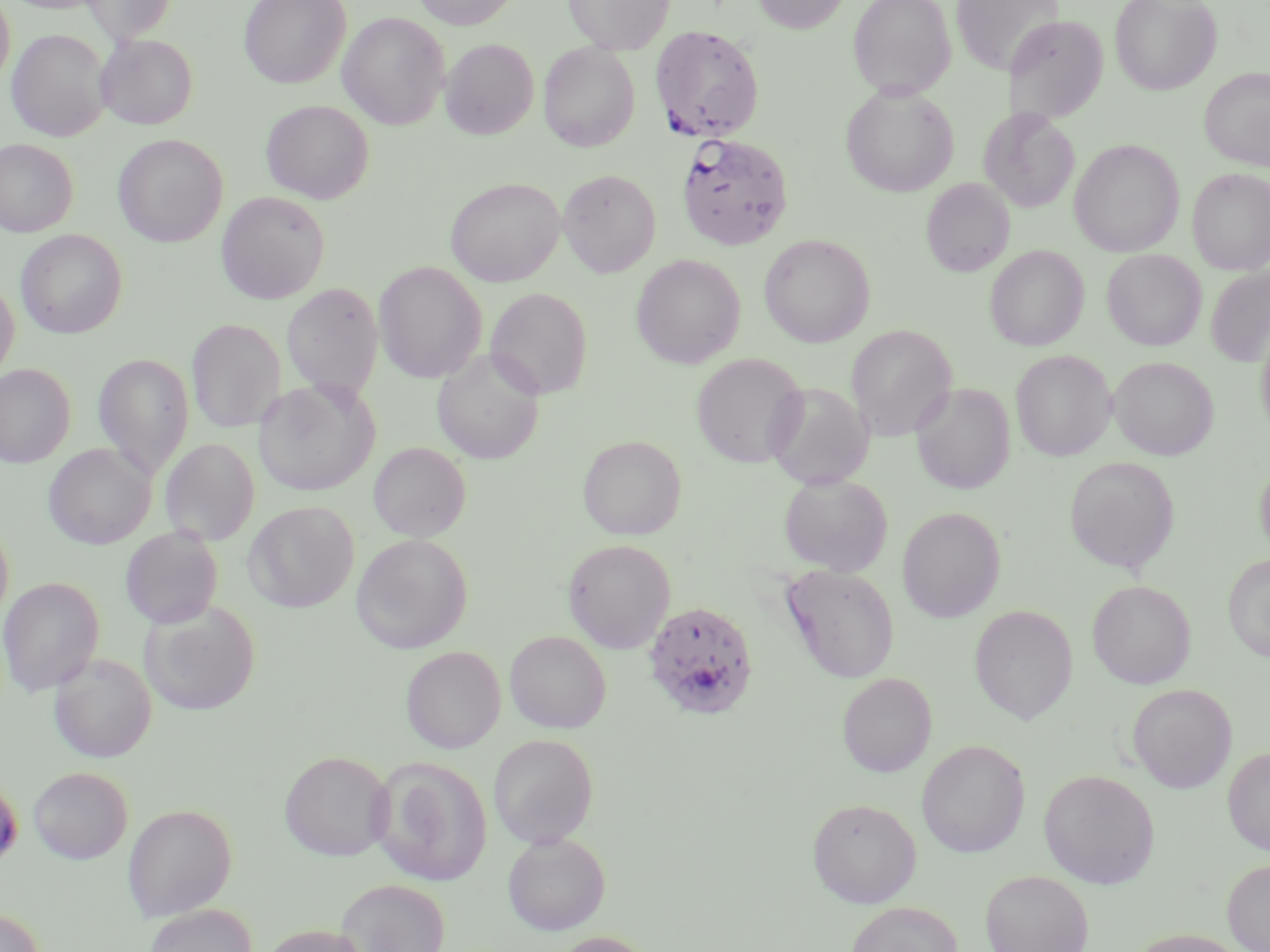

Approximate bounding boxes as named x1/y1/x2/y2 corners in pixels. Plasmodium falciparum-infected red blood cell locations: (x1=650, y1=25, x2=765, y2=142), (x1=676, y1=132, x2=793, y2=250), (x1=643, y1=600, x2=759, y2=720). Uninfected red blood cell locations: (x1=0, y1=0, x2=15, y2=89), (x1=80, y1=0, x2=177, y2=44), (x1=239, y1=0, x2=351, y2=88), (x1=413, y1=0, x2=519, y2=29), (x1=564, y1=0, x2=674, y2=54), (x1=751, y1=0, x2=853, y2=33), (x1=847, y1=0, x2=956, y2=99), (x1=950, y1=0, x2=1061, y2=74), (x1=1110, y1=0, x2=1222, y2=95), (x1=338, y1=12, x2=449, y2=130), (x1=1004, y1=15, x2=1109, y2=123), (x1=7, y1=28, x2=111, y2=141), (x1=96, y1=34, x2=198, y2=130), (x1=440, y1=38, x2=539, y2=139), (x1=539, y1=42, x2=640, y2=152), (x1=1199, y1=67, x2=1270, y2=170), (x1=841, y1=84, x2=959, y2=197), (x1=261, y1=100, x2=374, y2=203), (x1=979, y1=107, x2=1080, y2=213), (x1=113, y1=134, x2=228, y2=247), (x1=0, y1=138, x2=77, y2=237), (x1=1069, y1=139, x2=1185, y2=257), (x1=1188, y1=168, x2=1270, y2=276), (x1=558, y1=169, x2=661, y2=277), (x1=446, y1=177, x2=565, y2=286), (x1=921, y1=178, x2=1015, y2=277), (x1=216, y1=190, x2=331, y2=304), (x1=16, y1=229, x2=127, y2=339), (x1=759, y1=233, x2=875, y2=347), (x1=985, y1=245, x2=1089, y2=351), (x1=1102, y1=249, x2=1206, y2=351), (x1=631, y1=254, x2=746, y2=369), (x1=373, y1=261, x2=487, y2=383), (x1=1205, y1=267, x2=1270, y2=367), (x1=0, y1=279, x2=19, y2=383), (x1=281, y1=283, x2=383, y2=403), (x1=485, y1=287, x2=594, y2=400), (x1=186, y1=318, x2=286, y2=433), (x1=1255, y1=319, x2=1270, y2=441), (x1=846, y1=324, x2=957, y2=441), (x1=432, y1=349, x2=545, y2=464), (x1=1011, y1=350, x2=1116, y2=461), (x1=94, y1=352, x2=193, y2=480), (x1=691, y1=353, x2=808, y2=469), (x1=1109, y1=356, x2=1218, y2=460), (x1=0, y1=363, x2=75, y2=468), (x1=253, y1=378, x2=380, y2=496), (x1=765, y1=381, x2=874, y2=490), (x1=910, y1=382, x2=1015, y2=494), (x1=577, y1=435, x2=686, y2=540), (x1=160, y1=438, x2=260, y2=546), (x1=368, y1=442, x2=471, y2=543), (x1=44, y1=444, x2=155, y2=549), (x1=1063, y1=456, x2=1180, y2=573), (x1=1254, y1=458, x2=1270, y2=560), (x1=778, y1=473, x2=893, y2=576), (x1=244, y1=501, x2=359, y2=612), (x1=897, y1=507, x2=1006, y2=623), (x1=0, y1=518, x2=14, y2=627), (x1=120, y1=527, x2=224, y2=629), (x1=351, y1=533, x2=473, y2=653), (x1=563, y1=538, x2=676, y2=653), (x1=1222, y1=554, x2=1270, y2=663), (x1=781, y1=565, x2=900, y2=683), (x1=0, y1=576, x2=105, y2=696), (x1=1087, y1=580, x2=1196, y2=689), (x1=140, y1=602, x2=260, y2=716), (x1=970, y1=605, x2=1077, y2=724), (x1=505, y1=630, x2=611, y2=734), (x1=401, y1=646, x2=506, y2=753), (x1=49, y1=653, x2=157, y2=763), (x1=837, y1=673, x2=936, y2=777), (x1=1128, y1=684, x2=1237, y2=793), (x1=488, y1=734, x2=599, y2=848), (x1=916, y1=739, x2=1030, y2=858), (x1=1222, y1=747, x2=1270, y2=856), (x1=279, y1=750, x2=394, y2=861), (x1=369, y1=757, x2=492, y2=886), (x1=28, y1=767, x2=133, y2=864), (x1=1038, y1=769, x2=1159, y2=888), (x1=0, y1=777, x2=23, y2=871), (x1=807, y1=797, x2=922, y2=908), (x1=122, y1=803, x2=237, y2=921), (x1=502, y1=832, x2=610, y2=935), (x1=1222, y1=858, x2=1270, y2=952), (x1=980, y1=870, x2=1093, y2=952), (x1=335, y1=878, x2=451, y2=952), (x1=845, y1=901, x2=964, y2=952), (x1=144, y1=904, x2=257, y2=952), (x1=0, y1=907, x2=45, y2=952), (x1=258, y1=924, x2=374, y2=952), (x1=1126, y1=928, x2=1253, y2=952), (x1=549, y1=931, x2=657, y2=952). Slide-level diagnosis: Plasmodium falciparum. 1000x magnification. Thin blood film. Light microscopy. One field of a larger specimen. Image is 1270×952 pixels. May-Grünwald-Giemsa stain.